Report the malaria status of this cell.
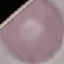
It is uninfected.

Photographed with a smartphone camera at the microscope eyepiece. Cell patch, automatically extracted from a larger field of view and resized to 64 × 64 pixels. Thin blood film. Giemsa stain.